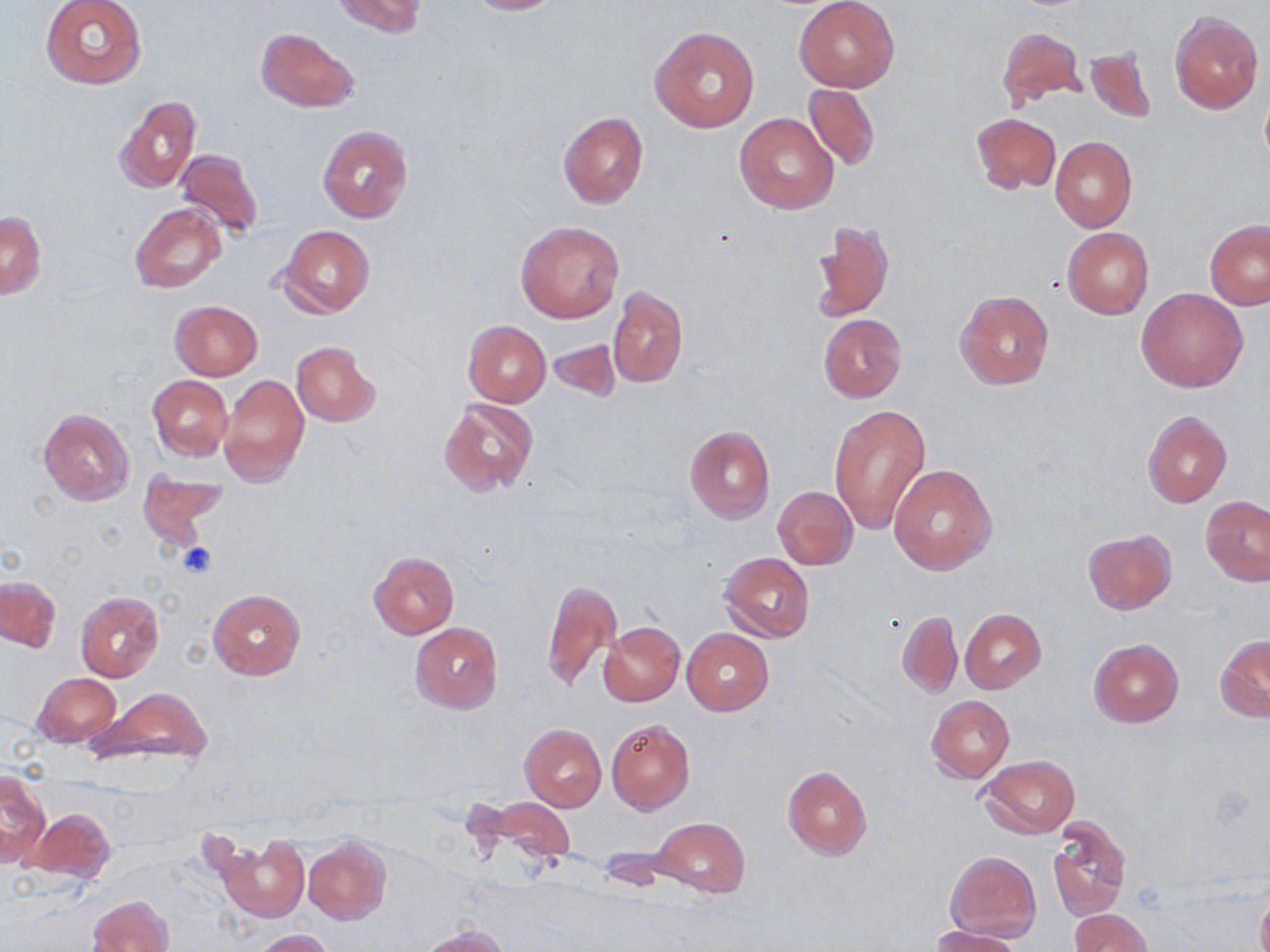

{
  "slide_level_diagnosis": "negative for blood parasites",
  "uninfected_red_blood_cell_locations": "approximate bounding boxes as [x1, y1, x2, y2] in pixels: [40, 0, 147, 90], [331, 0, 427, 37], [461, 0, 565, 14], [794, 1, 899, 92], [1169, 10, 1264, 114], [998, 25, 1085, 111], [650, 26, 759, 132], [256, 27, 359, 112], [1084, 45, 1156, 124], [802, 84, 880, 169], [115, 95, 201, 193], [557, 112, 649, 209], [735, 113, 838, 214], [971, 114, 1061, 194], [318, 125, 412, 222], [973, 128, 1135, 219], [1050, 137, 1136, 231], [174, 148, 264, 240], [130, 202, 227, 295], [1, 212, 45, 299], [810, 218, 895, 323], [1205, 218, 1270, 309], [515, 221, 624, 323], [278, 225, 375, 318], [1061, 228, 1153, 320], [608, 286, 688, 387], [1137, 288, 1248, 391], [955, 290, 1054, 390], [169, 300, 264, 381], [818, 313, 906, 403], [464, 321, 551, 406], [547, 335, 624, 402], [292, 342, 380, 427], [218, 374, 308, 488], [147, 375, 232, 460], [438, 397, 538, 494], [830, 404, 932, 533], [39, 407, 135, 506], [1143, 410, 1232, 507], [684, 425, 776, 524], [888, 463, 1000, 576], [136, 469, 228, 549], [771, 486, 857, 569], [1202, 495, 1269, 587], [1082, 529, 1176, 613], [369, 551, 459, 639], [720, 552, 815, 642], [1, 576, 61, 652], [542, 578, 621, 693], [208, 589, 305, 680], [74, 591, 165, 684], [961, 609, 1046, 692], [898, 611, 962, 697], [598, 622, 685, 706], [409, 623, 503, 712], [682, 629, 773, 715], [1217, 635, 1270, 721], [1088, 638, 1184, 727], [32, 673, 121, 747], [91, 688, 214, 767], [927, 696, 1014, 784], [606, 718, 695, 814], [519, 723, 606, 812], [977, 755, 1080, 838], [782, 766, 872, 860], [0, 768, 50, 868], [466, 795, 575, 871], [24, 807, 115, 885], [650, 817, 750, 898], [1047, 818, 1130, 920], [213, 832, 309, 922], [303, 837, 392, 925], [945, 850, 1040, 943], [1256, 889, 1270, 952], [88, 895, 174, 952], [1069, 909, 1151, 952], [931, 925, 1024, 952], [418, 926, 509, 952], [253, 929, 335, 952]",
  "magnification": "1000x",
  "preparation": "thin blood film",
  "field_of_view": "single",
  "stain": "May-Grünwald-Giemsa",
  "image_size": "1270×952 pixels",
  "modality": "optical microscopy"
}